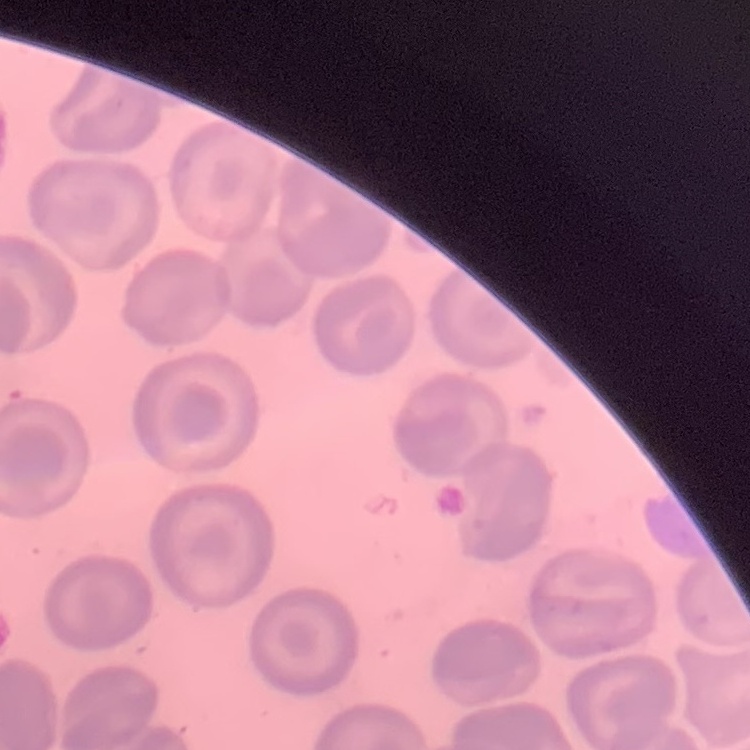
The red blood cells exhibit no rouleaux formation. Thin blood smear. Square crop of a larger photomicrograph. Field's or Giemsa stain.